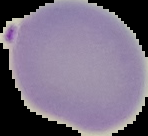

Image is 148×136 pixels. The area outside the segmented cell region is set to black. Malaria status: uninfected. From a thin blood film.